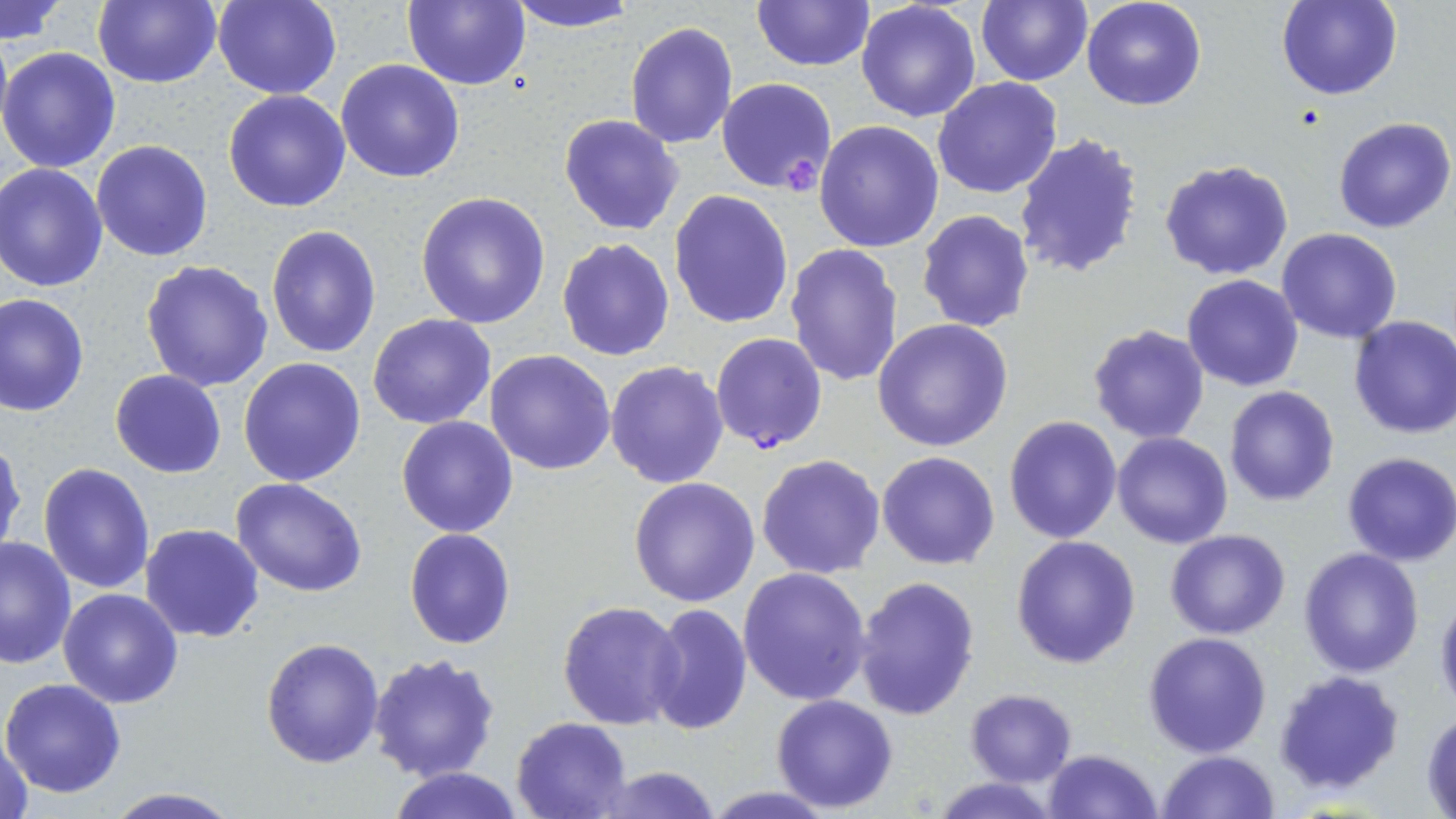
Summary:
  - Coordinate format: approximate bounding boxes as named x1/y1/x2/y2 corners in pixels
  - Platelet locations: (x1=782, y1=148, x2=822, y2=191)
  - Plasmodium falciparum-infected red blood cell locations: (x1=710, y1=331, x2=828, y2=454)
  - Uninfected red blood cell locations: (x1=92, y1=0, x2=222, y2=89), (x1=212, y1=0, x2=342, y2=99), (x1=402, y1=0, x2=530, y2=90), (x1=506, y1=0, x2=644, y2=31), (x1=750, y1=0, x2=874, y2=72), (x1=1080, y1=0, x2=1207, y2=111), (x1=1275, y1=0, x2=1403, y2=101), (x1=856, y1=1, x2=982, y2=121), (x1=975, y1=1, x2=1093, y2=86), (x1=1, y1=2, x2=70, y2=43), (x1=625, y1=21, x2=739, y2=150), (x1=0, y1=28, x2=12, y2=145), (x1=0, y1=46, x2=122, y2=173), (x1=336, y1=59, x2=466, y2=183), (x1=933, y1=77, x2=1063, y2=199), (x1=715, y1=79, x2=836, y2=193), (x1=222, y1=89, x2=351, y2=212), (x1=558, y1=113, x2=685, y2=236), (x1=1333, y1=117, x2=1456, y2=234), (x1=814, y1=119, x2=945, y2=252), (x1=1014, y1=131, x2=1146, y2=282), (x1=91, y1=140, x2=214, y2=261), (x1=1158, y1=158, x2=1294, y2=281), (x1=0, y1=163, x2=108, y2=292), (x1=669, y1=189, x2=795, y2=328), (x1=416, y1=190, x2=551, y2=328), (x1=917, y1=210, x2=1034, y2=332), (x1=264, y1=224, x2=381, y2=360), (x1=1276, y1=228, x2=1404, y2=344), (x1=555, y1=238, x2=675, y2=361), (x1=785, y1=242, x2=904, y2=387), (x1=140, y1=259, x2=276, y2=393), (x1=1183, y1=274, x2=1304, y2=391), (x1=0, y1=292, x2=90, y2=417), (x1=367, y1=314, x2=495, y2=428), (x1=1348, y1=315, x2=1456, y2=441), (x1=873, y1=318, x2=1014, y2=452), (x1=1087, y1=323, x2=1212, y2=444), (x1=485, y1=350, x2=616, y2=476), (x1=238, y1=357, x2=366, y2=486), (x1=605, y1=360, x2=728, y2=488), (x1=110, y1=370, x2=226, y2=478), (x1=1223, y1=385, x2=1340, y2=507), (x1=396, y1=415, x2=521, y2=537), (x1=1004, y1=415, x2=1123, y2=543), (x1=1113, y1=432, x2=1234, y2=549), (x1=0, y1=439, x2=25, y2=563), (x1=877, y1=451, x2=1001, y2=570), (x1=1341, y1=453, x2=1456, y2=567), (x1=755, y1=454, x2=886, y2=579), (x1=38, y1=461, x2=156, y2=595), (x1=629, y1=477, x2=761, y2=607), (x1=230, y1=478, x2=369, y2=599), (x1=140, y1=523, x2=266, y2=642), (x1=404, y1=527, x2=515, y2=649), (x1=1165, y1=529, x2=1291, y2=640), (x1=1012, y1=534, x2=1141, y2=669), (x1=0, y1=535, x2=76, y2=669), (x1=1298, y1=547, x2=1426, y2=679), (x1=739, y1=566, x2=873, y2=705), (x1=855, y1=575, x2=981, y2=724), (x1=58, y1=588, x2=184, y2=708), (x1=1434, y1=589, x2=1456, y2=713), (x1=555, y1=599, x2=686, y2=730), (x1=648, y1=604, x2=752, y2=735), (x1=1144, y1=631, x2=1271, y2=756), (x1=261, y1=637, x2=385, y2=768), (x1=368, y1=652, x2=501, y2=782), (x1=1272, y1=668, x2=1407, y2=798), (x1=1, y1=677, x2=127, y2=799), (x1=963, y1=688, x2=1077, y2=785), (x1=770, y1=694, x2=898, y2=812), (x1=1421, y1=708, x2=1455, y2=814), (x1=512, y1=716, x2=633, y2=818), (x1=1, y1=732, x2=37, y2=819), (x1=1044, y1=747, x2=1161, y2=818), (x1=1156, y1=750, x2=1280, y2=819), (x1=595, y1=765, x2=725, y2=819), (x1=387, y1=766, x2=527, y2=819), (x1=931, y1=777, x2=1062, y2=817), (x1=102, y1=788, x2=243, y2=818)
  - Slide-level diagnosis: Plasmodium falciparum
  - Modality: light microscopy
  - Field of view: single
  - Preparation: thin blood film
  - Stain: May-Grünwald-Giemsa
  - Image size: 1456×819 pixels
  - Magnification: 1000x